Mark where platelets are.
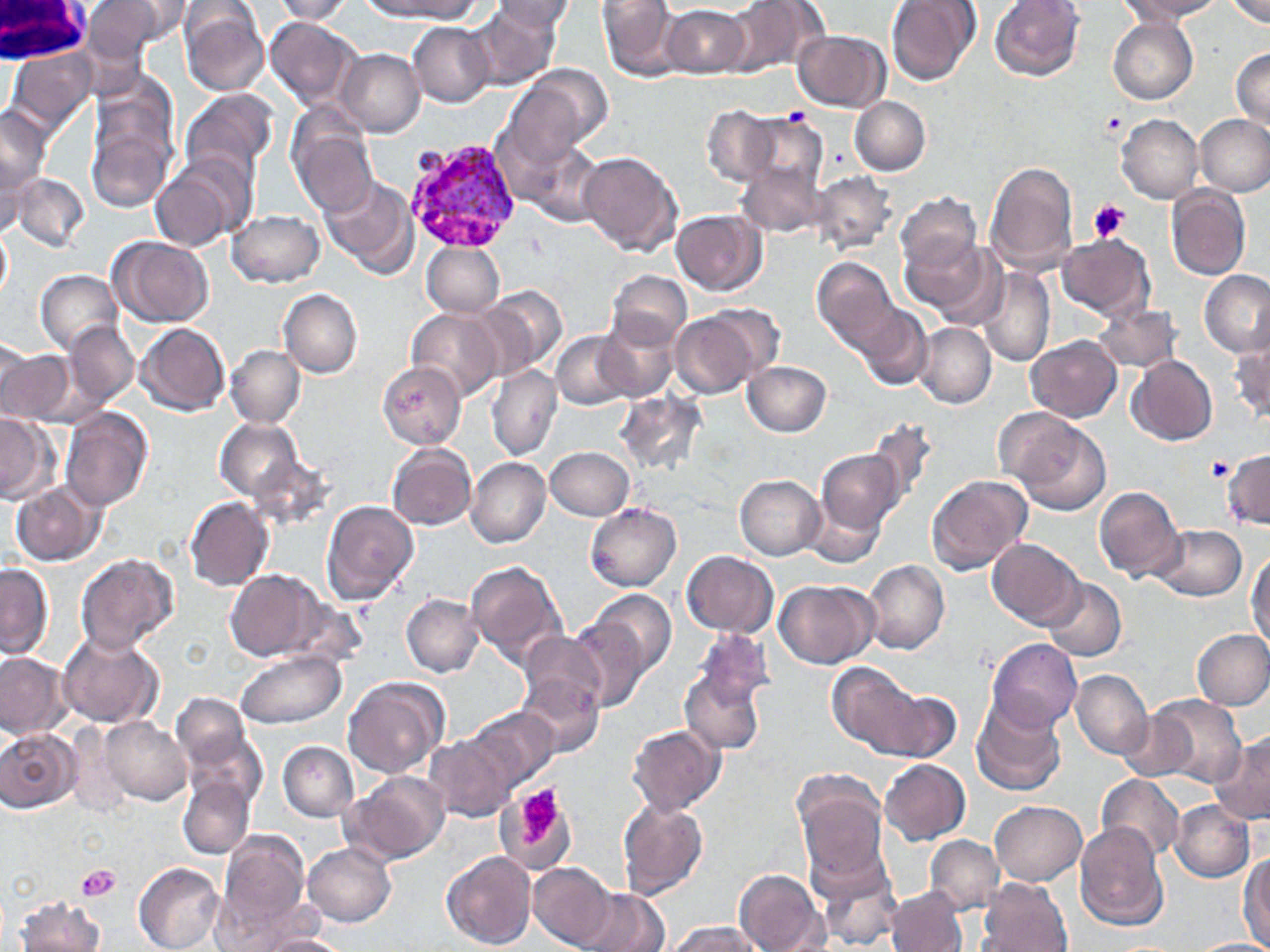

Approximate bounding boxes as [x1, y1, x2, y2] in pixels.
Platelets: [785, 106, 811, 127], [1101, 109, 1127, 139], [1088, 199, 1129, 245], [1207, 458, 1233, 482], [517, 784, 560, 844], [75, 863, 121, 901].

Plasmodium vivax-infected red blood cell locations: [406, 138, 522, 256]. Uninfected red blood cell locations: [80, 0, 175, 59], [270, 0, 356, 23], [367, 0, 479, 19], [597, 0, 684, 80], [721, 0, 829, 79], [885, 0, 979, 86], [990, 0, 1084, 81], [1120, 0, 1221, 22], [1226, 0, 1270, 26], [112, 1, 194, 44], [493, 1, 579, 32], [180, 2, 271, 97], [471, 5, 562, 90], [661, 5, 750, 80], [264, 16, 362, 110], [1108, 17, 1197, 104], [408, 22, 494, 107], [794, 30, 890, 111], [1230, 47, 1270, 130], [5, 49, 98, 142], [339, 49, 425, 136], [514, 64, 613, 154], [178, 88, 279, 188], [851, 96, 931, 175], [86, 99, 178, 216], [0, 104, 51, 205], [703, 104, 779, 186], [737, 113, 826, 194], [1116, 115, 1203, 204], [1196, 115, 1269, 195], [291, 121, 379, 217], [523, 142, 606, 226], [579, 151, 682, 255], [149, 155, 253, 252], [736, 158, 827, 240], [985, 161, 1078, 276], [811, 171, 896, 257], [11, 173, 90, 252], [319, 176, 417, 280], [1167, 185, 1251, 280], [898, 192, 979, 274], [228, 209, 326, 287], [672, 210, 767, 295], [0, 226, 11, 301], [900, 231, 995, 317], [1057, 232, 1155, 319], [109, 236, 214, 327], [423, 241, 505, 318], [813, 257, 898, 354], [976, 266, 1056, 369], [35, 270, 125, 355], [607, 270, 692, 347], [1199, 271, 1269, 355], [477, 287, 567, 378], [279, 289, 363, 378], [1093, 301, 1180, 374], [856, 305, 934, 391], [407, 307, 505, 401], [670, 307, 767, 397], [596, 315, 678, 404], [65, 322, 137, 407], [136, 322, 230, 416], [914, 323, 996, 408], [551, 331, 632, 408], [1027, 336, 1121, 421], [1229, 337, 1270, 427], [0, 344, 76, 428], [227, 345, 304, 427], [1129, 355, 1218, 446], [377, 361, 467, 450], [743, 361, 832, 435], [487, 366, 562, 461], [618, 389, 701, 473], [60, 409, 152, 513], [0, 412, 57, 503], [1004, 412, 1109, 518], [864, 415, 939, 506], [215, 417, 304, 502], [388, 442, 477, 531], [547, 446, 636, 520], [1223, 447, 1270, 531], [249, 449, 337, 530], [816, 449, 904, 532], [467, 457, 549, 547], [341, 474, 426, 569], [926, 474, 1032, 575], [735, 475, 825, 560], [12, 479, 102, 566], [1094, 486, 1185, 581], [805, 496, 883, 567], [185, 497, 273, 592], [321, 500, 419, 606], [584, 503, 681, 593], [1150, 525, 1247, 603], [990, 538, 1084, 628], [1246, 549, 1269, 650], [682, 550, 778, 638], [75, 553, 178, 654], [466, 558, 568, 671], [864, 560, 950, 655], [0, 564, 53, 658], [225, 567, 327, 661], [1043, 578, 1127, 662], [774, 579, 879, 669], [587, 589, 677, 681], [403, 593, 484, 677], [567, 611, 655, 714], [697, 626, 777, 711], [1192, 628, 1270, 709], [59, 632, 162, 729], [520, 633, 608, 718], [988, 637, 1081, 731], [234, 649, 346, 730], [1, 652, 72, 738], [678, 659, 769, 758], [826, 661, 927, 758], [1071, 670, 1152, 758], [515, 671, 606, 759], [342, 677, 449, 780], [881, 688, 964, 763], [971, 694, 1068, 796], [1147, 695, 1248, 786], [171, 699, 266, 809], [1118, 704, 1205, 785], [468, 706, 558, 794], [99, 717, 193, 806], [627, 725, 726, 815], [0, 727, 82, 816], [427, 732, 517, 822], [1210, 737, 1270, 824], [278, 741, 360, 821], [879, 759, 972, 845], [791, 767, 887, 876], [343, 771, 450, 866], [1095, 774, 1183, 863], [178, 777, 254, 858], [489, 791, 577, 874], [616, 798, 709, 899], [1170, 800, 1254, 881], [991, 801, 1087, 887], [1074, 823, 1170, 931], [215, 828, 311, 933], [925, 835, 1003, 914], [302, 841, 397, 927], [439, 853, 535, 951], [1238, 854, 1270, 948], [812, 858, 904, 949], [134, 862, 225, 952], [528, 862, 615, 949], [734, 870, 829, 951], [974, 877, 1072, 952], [574, 887, 670, 952], [885, 887, 968, 952], [14, 893, 105, 952], [667, 921, 764, 952], [264, 934, 350, 952], [1191, 938, 1270, 952]. White blood cell locations: [0, 0, 90, 64]. Slide-level diagnosis: Plasmodium vivax. One field of a larger specimen. Optical microscopy. Image is 1270×952 pixels. 1000x magnification. May-Grünwald-Giemsa stain. Thin blood smear.